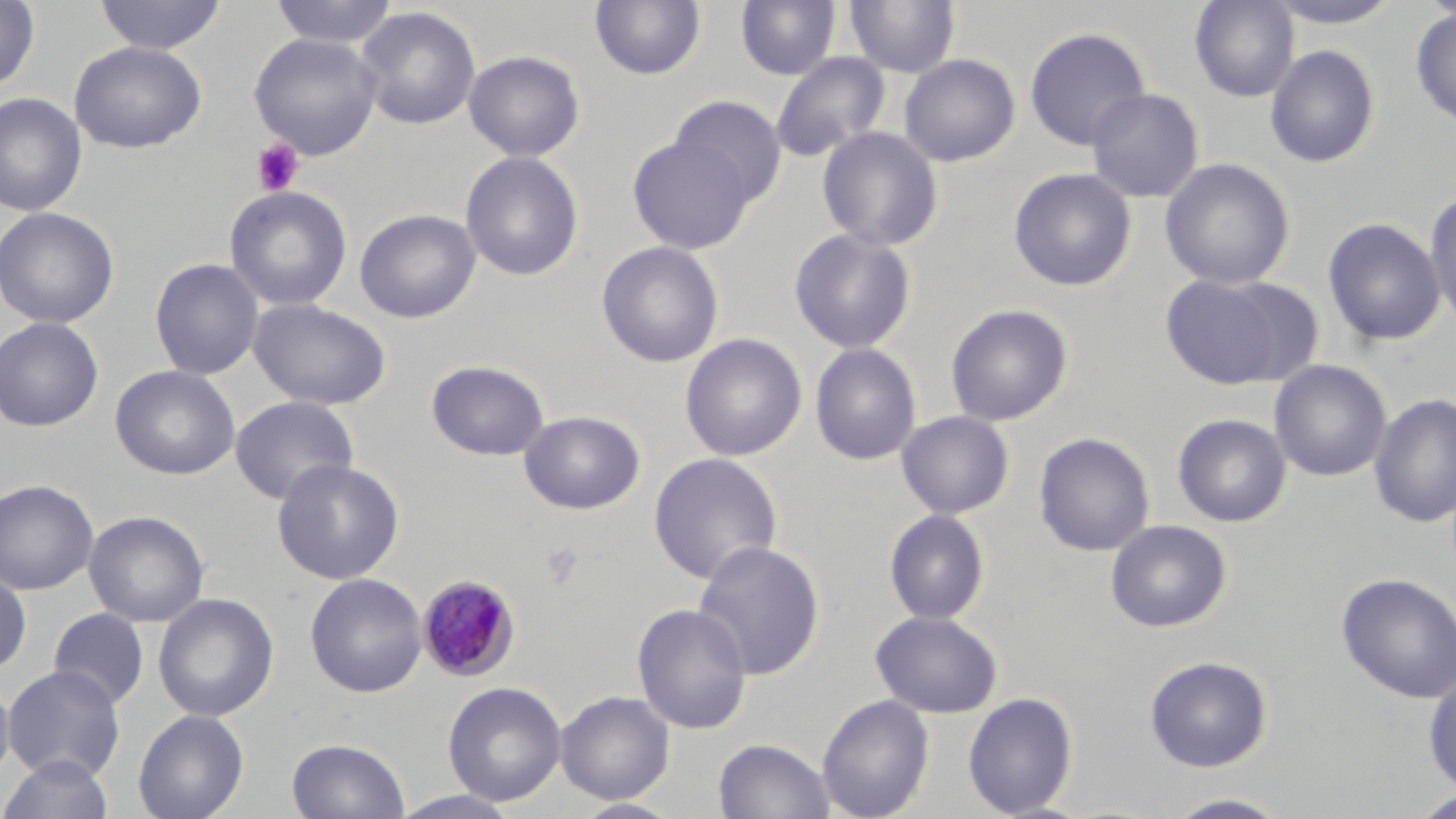 Approximate bounding boxes as (x1,y1)-(x2,y2) corner pairs in pixels. Plasmodium malariae-infected red blood cell locations: (416,574)-(521,682). Platelet locations: (250,137)-(305,196), (539,541)-(585,589). Uninfected red blood cell locations: (0,0)-(40,92), (94,0)-(227,55), (269,0)-(400,48), (590,0)-(706,81), (844,0)-(960,78), (1189,0)-(1299,102), (1263,0)-(1407,28), (736,1)-(840,80), (354,6)-(481,130), (1410,7)-(1456,127), (1024,26)-(1150,150), (248,32)-(383,160), (69,41)-(207,153), (1265,44)-(1380,168), (464,50)-(585,161), (771,52)-(890,161), (899,53)-(1020,167), (1085,88)-(1204,203), (0,92)-(87,217), (669,95)-(787,205), (817,126)-(944,252), (627,135)-(755,254), (460,151)-(584,281), (1160,158)-(1295,289), (1008,167)-(1137,291), (223,185)-(352,311), (1423,191)-(1456,329), (0,206)-(119,328), (355,208)-(481,323), (1322,217)-(1447,346), (788,228)-(917,353), (596,240)-(725,368), (149,258)-(264,380), (1159,272)-(1311,390), (248,298)-(392,410), (945,303)-(1073,426), (0,316)-(105,432), (680,333)-(807,461), (809,342)-(922,466), (426,360)-(550,461), (1268,360)-(1392,482), (110,365)-(240,480), (1368,393)-(1456,528), (230,396)-(359,505), (519,410)-(646,515), (896,410)-(1015,519), (1172,413)-(1292,527), (1034,432)-(1155,557), (648,452)-(783,585), (271,458)-(405,585), (0,479)-(99,595), (884,509)-(990,625), (84,510)-(209,628), (1105,520)-(1232,632), (691,540)-(826,680), (0,569)-(32,676), (304,573)-(428,698), (1336,573)-(1456,704), (153,593)-(279,722), (632,603)-(753,734), (48,607)-(149,710), (871,611)-(1002,717), (1144,655)-(1273,772), (2,664)-(126,781), (1423,671)-(1456,796), (0,677)-(16,787), (443,681)-(567,806), (556,690)-(675,805), (962,692)-(1078,818), (816,694)-(934,819), (132,709)-(249,819), (286,737)-(410,819), (713,737)-(836,819), (1,753)-(115,819), (1411,789)-(1456,818), (387,790)-(523,819), (1163,792)-(1293,819), (571,798)-(686,819). Slide-level diagnosis: Plasmodium malariae. 1000x magnification. Single field of view. Thin blood smear. Image is 1456×819 pixels. Light microscopy. May-Grünwald-Giemsa stain.